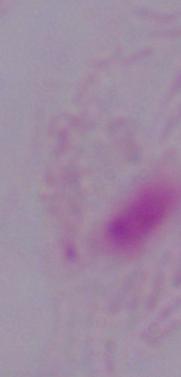 Photomicrograph. A trichomonad is shown. Captured at 1000x magnification.